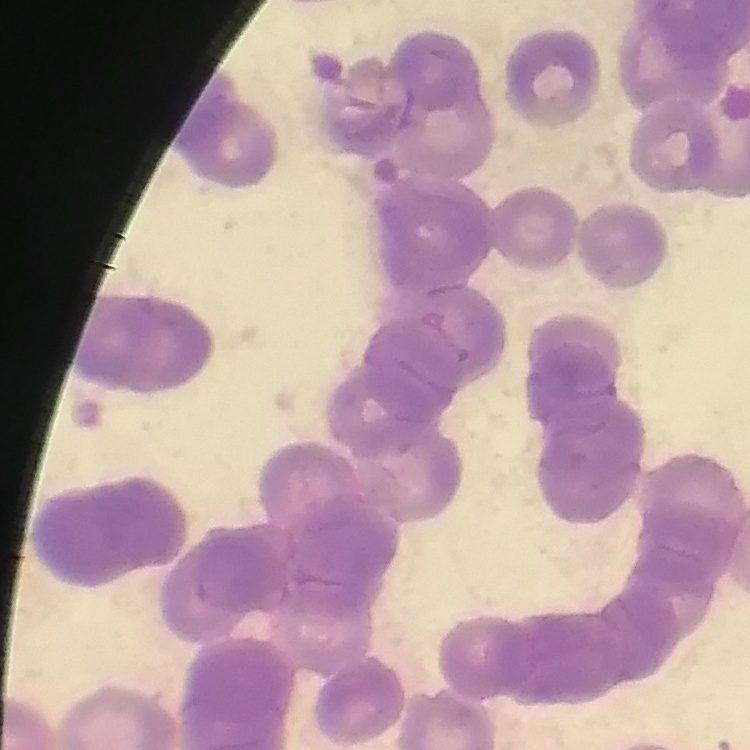 The erythrocytes show rouleaux formation. Square crop of a larger photomicrograph. Thin peripheral smear. Field's or Giemsa stain.